Report the malaria status of this cell.
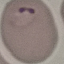
It is parasitized.

Cell patch, automatically extracted from a larger field of view and resized to 64 × 64 pixels. Giemsa stain. Photographed with a smartphone camera at the microscope eyepiece. Thin blood smear.